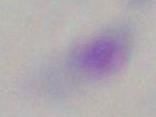
{
  "modality": "micrograph",
  "identification": "Toxoplasma gondii",
  "magnification": "1000x"
}